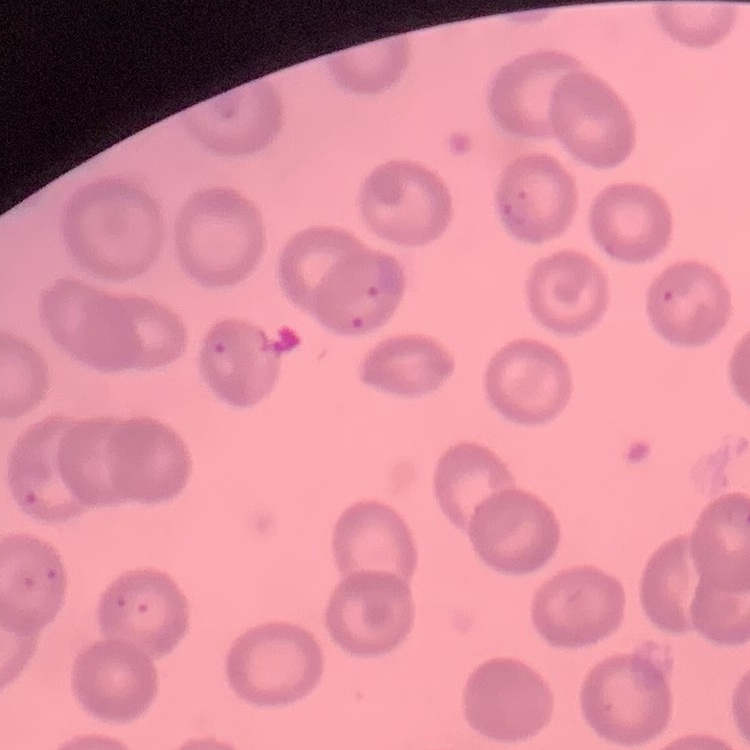

erythrocyte morphology = no rouleaux formation
image type = one tile cut from a larger photomicrograph
preparation = thin peripheral smear
stain = Field's or Giemsa